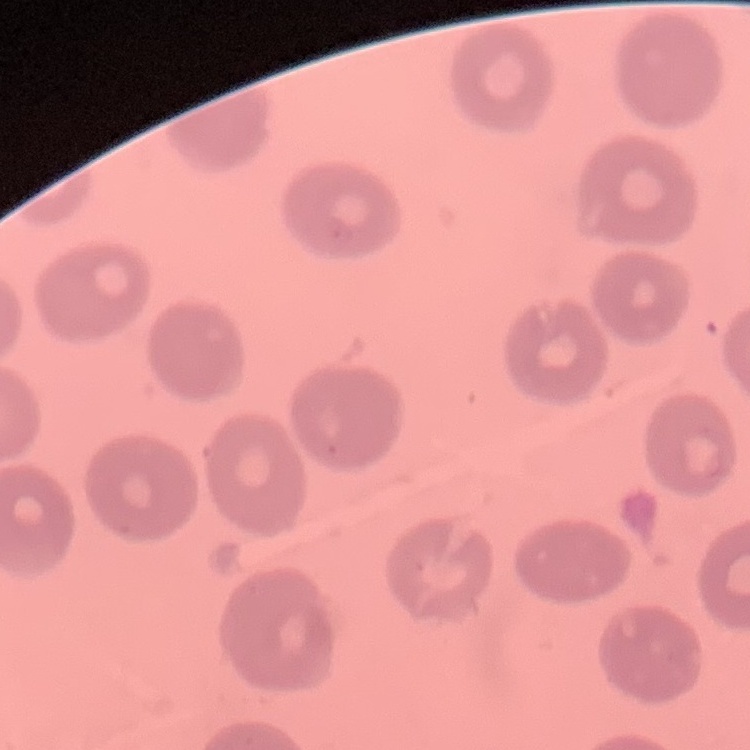
red blood cell morphology = no rouleaux formation
preparation = thin blood smear
image type = one tile cut from a larger photomicrograph
stain = Field's or Giemsa